Name the parasite shown.
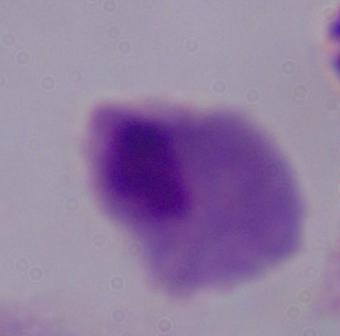
A trichomonad.

Micrograph. Captured at 1000x magnification.